Comment on the morphology of the erythrocytes.
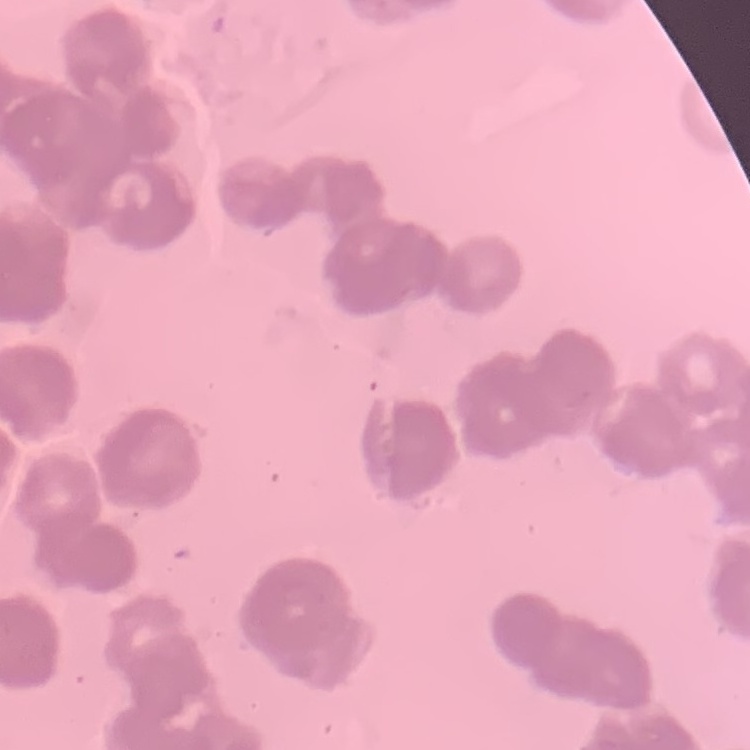
Rouleaux formation.

Thin peripheral smear. One tile cut from a larger photomicrograph. Field's or Giemsa stain.